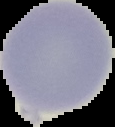

Cell region segmented out of the field of view; the surrounding area is masked to black. Malaria status: uninfected. Image is 115×127 pixels. From a thin blood smear.